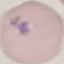

Result: malaria parasites detected. Thin blood film. Cell patch, automatically extracted from a larger field of view and resized to 64 × 64 pixels. Photographed with a smartphone camera at the microscope eyepiece. Giemsa-stained preparation.